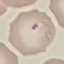

Summary:
  - Result: malaria parasites detected
  - Capture: smartphone camera at the microscope eyepiece
  - Preparation: thin blood film
  - Image type: automatically extracted cell patch, resized to 64 × 64 pixels
  - Stain: Giemsa